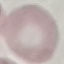

Malaria status: uninfected. Automatically extracted cell patch, resized to 64 × 64 pixels. Photographed with a smartphone camera at the microscope eyepiece. Thin blood smear. Giemsa stain.